Outline each Plasmodium vivax-infected red blood cell.
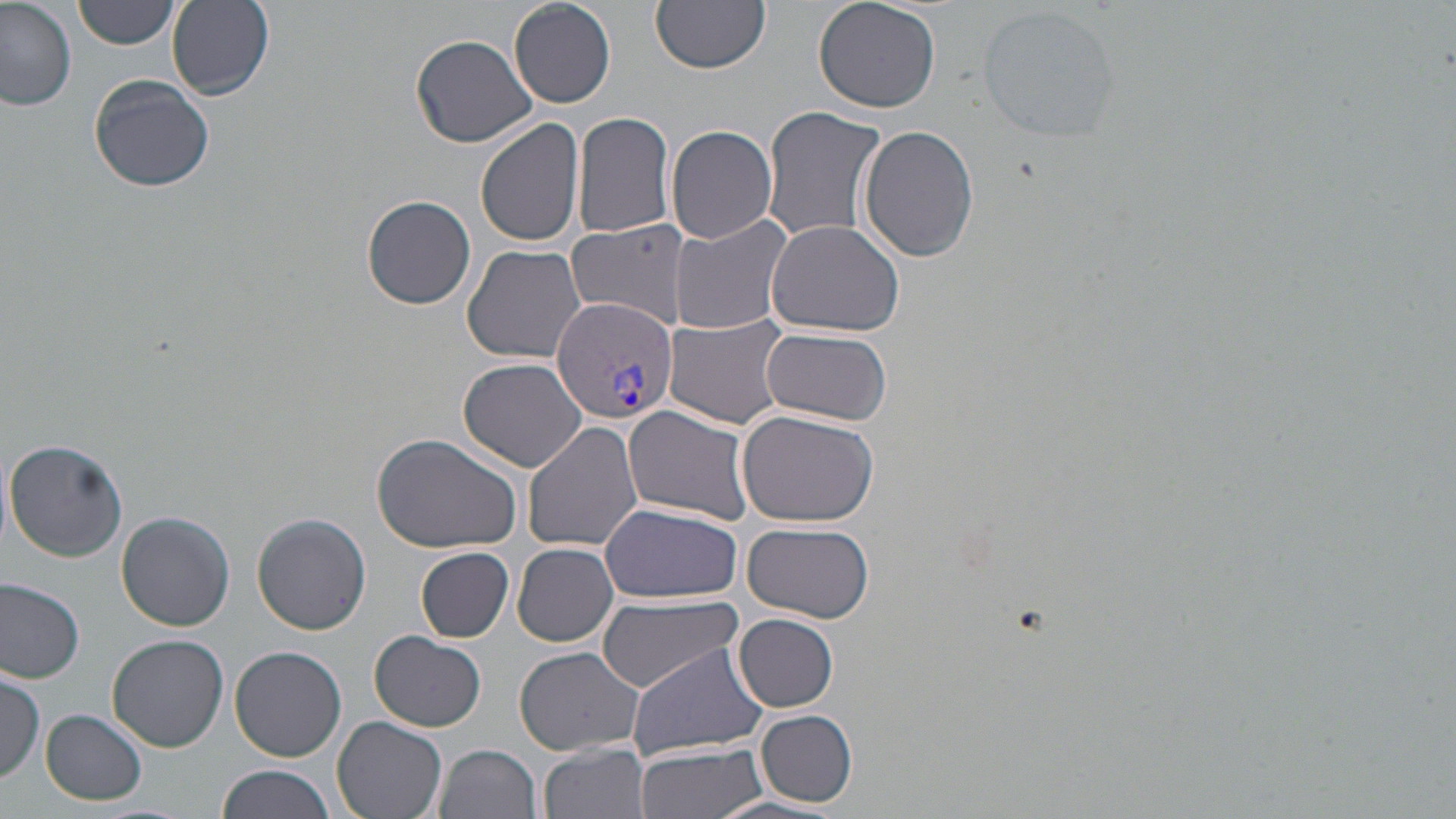
Approximate bounding boxes as (x1, y1, x2, y2) in pixels.
Plasmodium vivax-infected red blood cells: (550, 297, 676, 426).

Summary:
  - Uninfected red blood cell locations: (74, 0, 180, 49), (510, 0, 616, 107), (653, 0, 769, 73), (813, 0, 943, 114), (0, 1, 78, 110), (164, 2, 275, 101), (978, 5, 1120, 142), (409, 33, 538, 148), (87, 75, 215, 193), (760, 105, 886, 246), (571, 110, 679, 242), (477, 118, 587, 247), (665, 124, 778, 244), (860, 127, 980, 264), (362, 194, 477, 310), (672, 213, 795, 336), (765, 219, 907, 338), (566, 221, 685, 329), (463, 246, 585, 363), (664, 318, 788, 427), (760, 327, 892, 425), (457, 357, 588, 472), (624, 406, 756, 525), (737, 409, 881, 530), (522, 421, 644, 552), (371, 430, 522, 553), (4, 438, 128, 562), (600, 503, 741, 604), (116, 511, 234, 630), (252, 513, 370, 636), (740, 520, 875, 623), (513, 543, 618, 646), (416, 546, 515, 642), (0, 576, 85, 681), (596, 597, 744, 691), (734, 613, 840, 712), (370, 631, 487, 731), (108, 635, 230, 752), (625, 643, 771, 763), (230, 644, 347, 762), (513, 645, 646, 757), (0, 670, 45, 782), (41, 709, 147, 805), (755, 709, 858, 807), (332, 716, 449, 819), (539, 742, 653, 819), (635, 744, 769, 819), (437, 745, 542, 819), (216, 764, 334, 819), (705, 793, 845, 818)
  - Slide-level diagnosis: Plasmodium vivax
  - Field of view: single
  - Preparation: thin blood smear
  - Image size: 1456×819 pixels
  - Modality: light microscopy
  - Magnification: 1000x
  - Stain: May-Grünwald-Giemsa